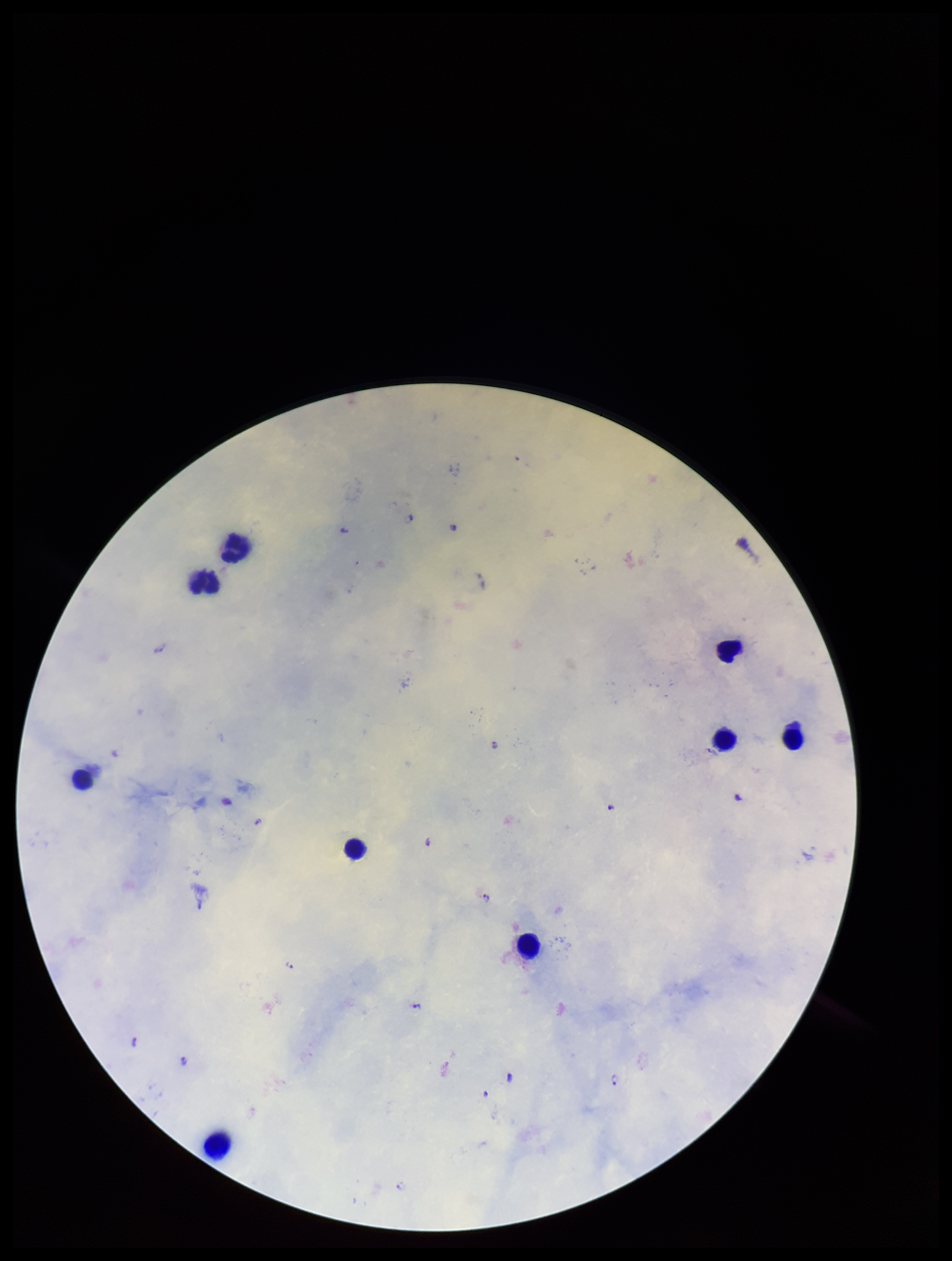

Leukocyte count: 9. Patient malaria status: positive. Plasmodium parasites: detected. Smartphone photograph taken through the eyepiece of a microscope. Preparation: thick blood smear. Image is 952×1261 pixels. Parasite count: 14. Single field of view. Stained with Giemsa. Species reported for this patient: Plasmodium falciparum.